Name the parasite shown.
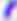

Toxoplasma gondii.

Summary:
  - Modality: micrograph
  - Magnification: 400x